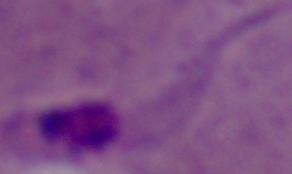 Micrograph. A Leishmania parasite is shown. Captured at 1000x magnification.